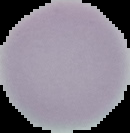
Summary:
  - Image type: cell region segmented out of the field of view; surrounding area masked to black
  - Preparation: thin blood film
  - Image size: 130×133 pixels
  - Result: negative for malaria parasites